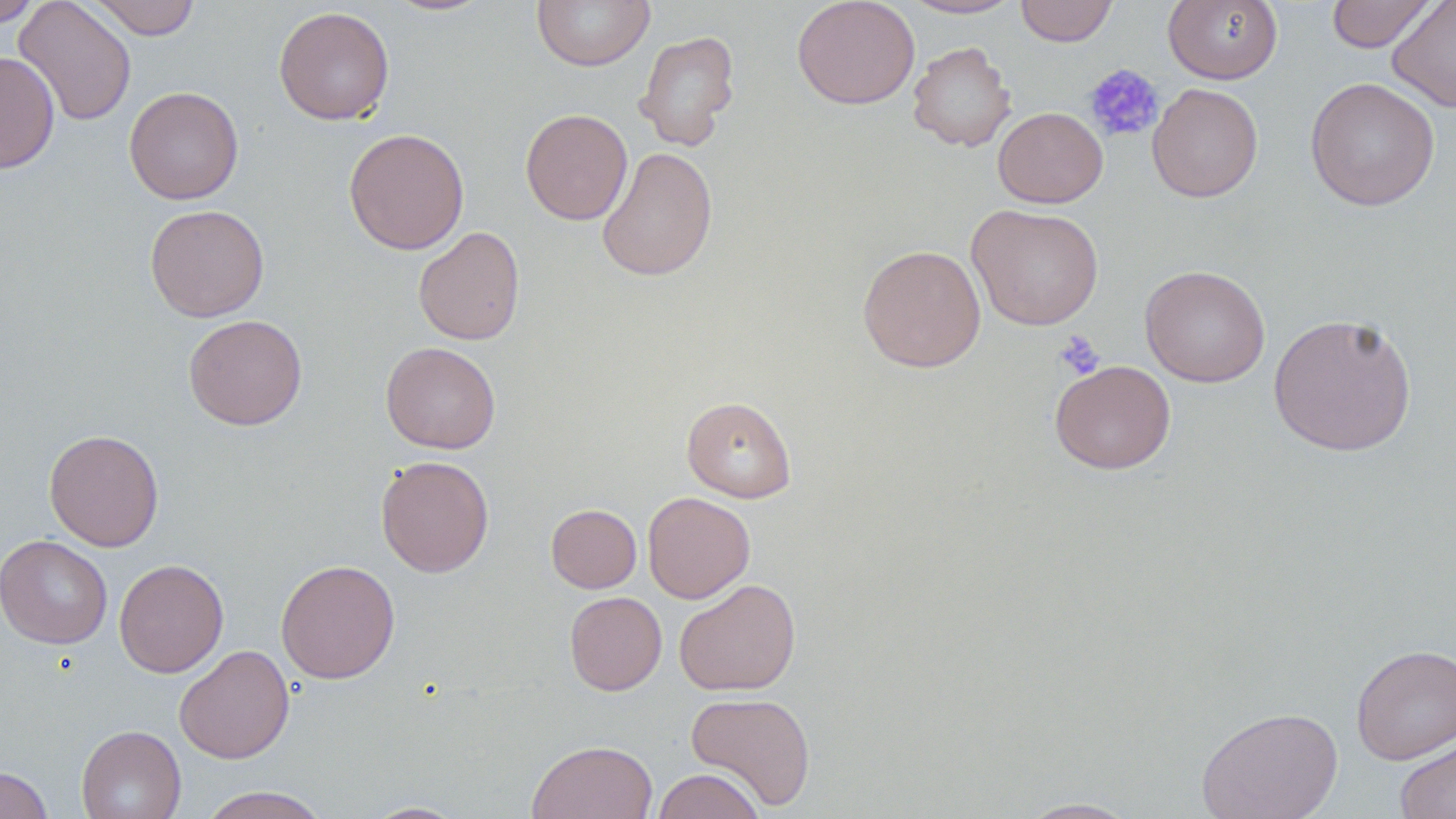

slide_level_diagnosis: no evidence of blood parasites
uninfected_red_blood_cell_locations: 'approximate bounding boxes as [x1, y1, x2, y2] in pixels: [0, 0, 42, 27], [14, 0, 137, 126], [88, 0, 201, 39], [382, 0, 498, 17], [532, 0, 654, 71], [792, 0, 920, 110], [901, 0, 1023, 19], [1014, 0, 1118, 46], [1163, 0, 1283, 84], [1326, 0, 1436, 53], [1387, 0, 1456, 113], [273, 6, 395, 125], [634, 29, 740, 151], [907, 41, 1017, 152], [0, 51, 60, 174], [1304, 76, 1440, 211], [1147, 83, 1263, 202], [124, 85, 244, 205], [993, 107, 1107, 208], [520, 108, 633, 225], [343, 128, 469, 255], [596, 146, 718, 282], [144, 204, 270, 322], [967, 204, 1104, 330], [413, 226, 525, 345], [857, 244, 986, 372], [1140, 264, 1270, 387], [1267, 312, 1418, 457], [183, 314, 308, 430], [380, 342, 501, 454], [1050, 359, 1176, 474], [681, 395, 797, 503], [44, 429, 164, 551], [375, 455, 495, 578], [642, 492, 755, 603], [546, 504, 642, 593], [0, 534, 113, 649], [114, 558, 229, 678], [276, 559, 400, 684], [674, 578, 801, 696], [564, 591, 667, 695], [1351, 643, 1456, 765], [174, 644, 294, 764], [686, 691, 816, 811], [1196, 705, 1343, 818], [76, 725, 186, 819], [1394, 736, 1456, 819], [526, 740, 659, 819], [0, 765, 53, 819], [652, 768, 764, 819], [197, 786, 330, 819], [1018, 797, 1141, 818], [361, 800, 469, 818]'
preparation: thin blood film
modality: light microscopy
stain: May-Grünwald-Giemsa
magnification: 1000x
field_of_view: one of a larger specimen
platelet_locations: 'approximate bounding boxes as [x1, y1, x2, y2] in pixels: [1084, 63, 1164, 143], [1054, 330, 1105, 379]'
image_size: 1456×819 pixels